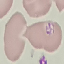
Summary:
  - Malaria status: uninfected
  - Capture: smartphone through the microscope eyepiece
  - Image type: automatically extracted cell patch, resized to 64 × 64 pixels
  - Preparation: thin blood smear
  - Stain: Giemsa